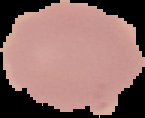

Summary:
  - Preparation: thin blood film
  - Image type: segmented cell region with the area outside set to black
  - Malaria status: uninfected
  - Image size: 145×118 pixels